Assess this cell for malaria.
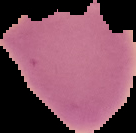
It is uninfected.

Summary:
  - Image type: cell region segmented out of the field of view; surrounding area masked to black
  - Image size: 136×133 pixels
  - Preparation: thin blood film